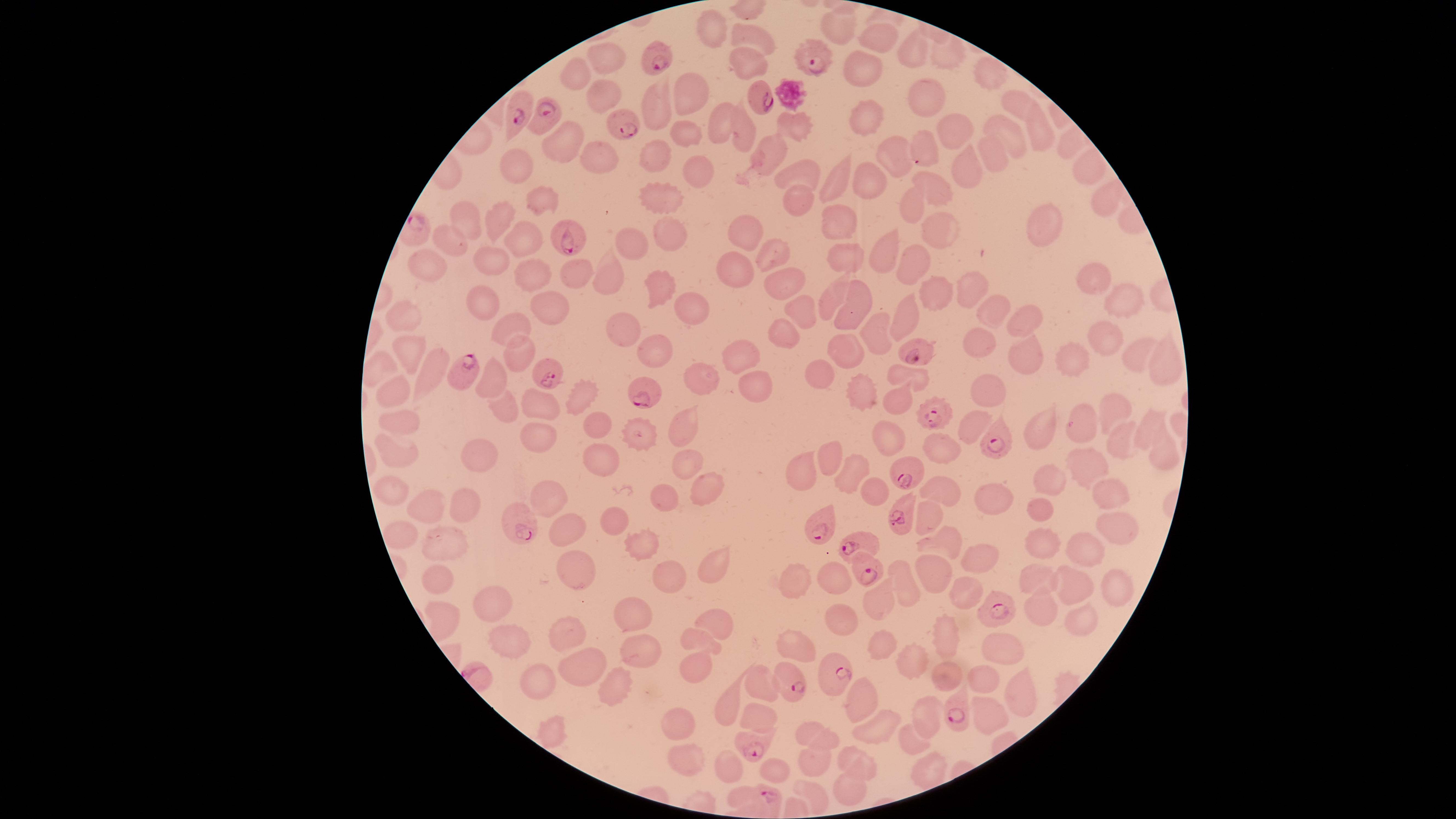
parasitized red blood cells = approximate marker points as [x, y] in pixels: [811, 54], [657, 57], [760, 100], [519, 110], [546, 119], [624, 126], [565, 241], [919, 353], [546, 370], [462, 371], [647, 395], [934, 413], [1000, 440], [901, 472], [898, 518], [517, 525], [820, 528], [859, 545], [868, 572], [994, 614], [832, 674], [793, 681], [951, 713], [752, 747], [772, 798]
preparation = thin blood smear
uninfected red blood cells = approximate marker points as [x, y] in pixels: [709, 23], [843, 31], [758, 34], [879, 38], [911, 54], [737, 57], [947, 58], [608, 62], [861, 68], [572, 74], [985, 78], [688, 92], [927, 94], [658, 102], [598, 103], [1018, 103], [862, 114], [720, 121], [742, 128], [1036, 129], [795, 130], [683, 132], [1002, 133], [564, 135], [958, 135], [924, 142], [996, 153], [597, 154], [653, 154], [897, 154], [773, 155], [516, 167], [689, 167], [1083, 169], [969, 170], [804, 175], [841, 179], [868, 181], [934, 188], [660, 199], [913, 202], [793, 203], [1100, 203], [542, 207], [464, 220], [500, 222], [668, 225], [836, 225], [936, 226], [750, 230], [1039, 230], [521, 239], [448, 241], [634, 244], [887, 251], [778, 253], [842, 253], [496, 257], [919, 262], [728, 268], [430, 271], [574, 271], [527, 272], [609, 278], [785, 278], [1092, 278], [662, 286], [976, 291], [937, 294], [837, 301], [1120, 301], [476, 305], [861, 305], [693, 308], [800, 309], [542, 312], [1002, 312], [409, 313], [912, 316], [1020, 321], [508, 323], [1105, 330], [626, 332], [879, 332], [786, 333], [983, 341], [662, 346], [413, 350], [846, 353], [514, 354], [1035, 355], [1136, 356], [742, 357], [1074, 358], [1171, 363], [434, 370], [822, 373], [700, 375], [915, 376], [496, 381], [394, 388], [752, 388], [985, 391], [865, 393], [579, 397], [889, 399], [506, 409], [537, 409], [1111, 409], [1084, 421], [399, 422], [686, 426], [1045, 426], [1148, 426], [594, 427], [964, 429], [642, 433], [884, 434], [1116, 438], [535, 443], [937, 449], [395, 455], [1156, 456], [480, 457], [598, 458], [835, 458], [684, 460], [1085, 464], [807, 467], [853, 472], [1047, 477], [707, 487], [872, 489], [1106, 492], [392, 493], [947, 493], [986, 494], [546, 495], [664, 497], [425, 507], [461, 510], [1044, 510], [929, 519], [617, 522], [1115, 528], [568, 532], [403, 534], [946, 538], [446, 541], [1039, 542], [638, 547], [1076, 550], [976, 554], [709, 569], [435, 571], [935, 572], [576, 576], [829, 577], [1042, 578], [791, 579], [905, 579], [669, 580], [1080, 583], [1106, 585], [963, 590], [486, 602], [881, 602], [1040, 608], [636, 616], [1076, 617], [445, 620], [841, 621], [715, 624], [942, 634], [570, 635], [506, 639], [697, 639], [883, 644], [637, 647], [799, 648], [1001, 650], [913, 663], [696, 668], [579, 672], [943, 680], [983, 680], [538, 681], [613, 684], [762, 684], [1017, 687], [860, 692], [722, 698], [985, 717], [918, 718], [756, 720], [677, 726], [877, 729], [549, 732], [817, 737], [909, 742], [853, 759], [726, 760], [684, 761], [772, 769], [815, 770], [846, 791], [741, 795]
presence = malaria parasites detected
capture = smartphone photograph through the microscope eyepiece
stain = Giemsa
species = Plasmodium falciparum
image size = 1456×819 pixels
field of view = single
visible region = circular